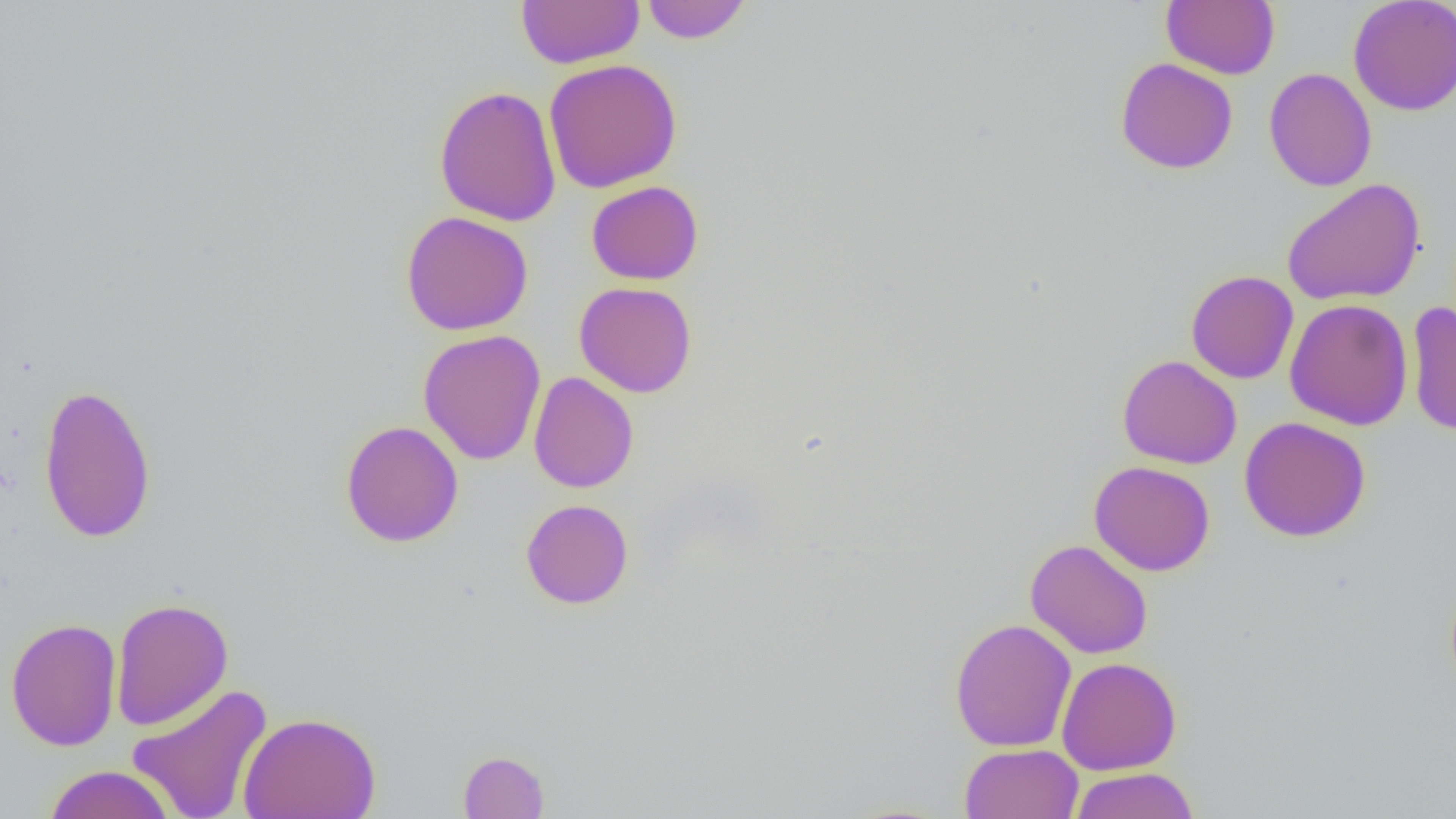

slide-level diagnosis = no evidence of blood parasites
field of view = single
magnification = 1000x
uninfected red blood cell locations = approximate bounding boxes as (x1,y1)-(x2,y2) corner pairs in pixels: (516,0)-(645,69), (641,0)-(752,43), (1161,0)-(1280,79), (1348,0)-(1456,116), (1115,58)-(1238,174), (543,59)-(682,193), (1263,67)-(1377,192), (434,85)-(562,227), (1281,179)-(1425,306), (586,180)-(703,285), (400,211)-(534,335), (1186,270)-(1299,383), (574,281)-(697,398), (1284,299)-(1413,430), (1406,302)-(1456,437), (418,329)-(546,465), (1117,355)-(1242,469), (528,371)-(638,493), (38,382)-(157,544), (1239,417)-(1371,542), (340,420)-(464,547), (1089,460)-(1215,576), (521,499)-(634,609), (1025,540)-(1153,659), (110,597)-(233,730), (5,617)-(122,751), (949,618)-(1077,751), (1056,656)-(1182,775), (127,683)-(273,819), (238,711)-(381,819), (959,743)-(1084,819), (458,750)-(550,818), (43,765)-(176,818), (1068,767)-(1199,819)
modality = light microscopy
preparation = thin blood film
image size = 1456×819 pixels